Classify this cell by malaria status.
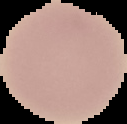
Uninfected.

Summary:
  - Preparation: thin blood smear
  - Image type: segmented cell region with the area outside set to black
  - Image size: 127×124 pixels